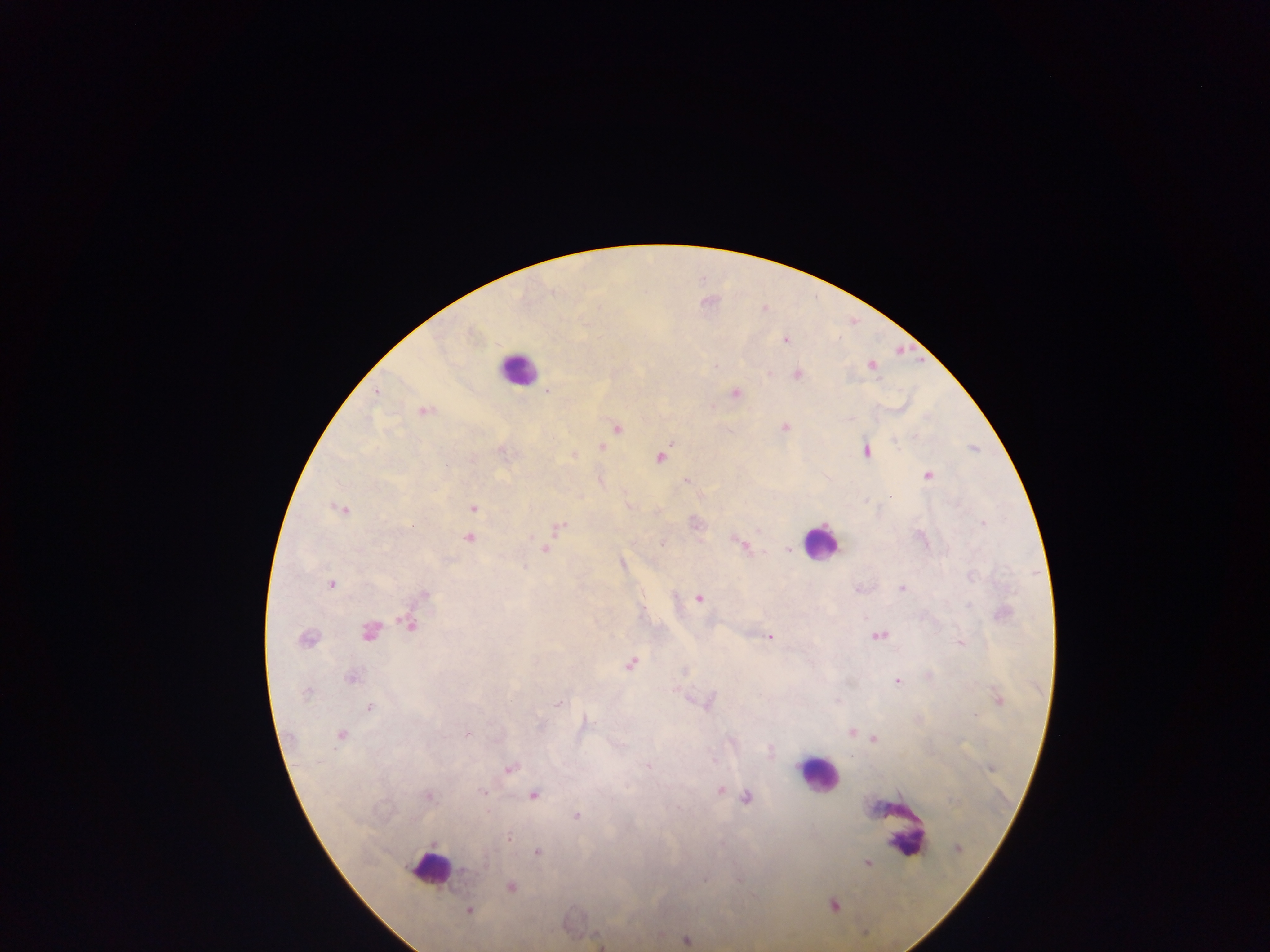
Approximate centers as [x, y] in pixels. Malaria parasite locations: [764, 309], [785, 340], [716, 365], [871, 365], [798, 374], [377, 391], [547, 391], [735, 393], [424, 412], [784, 427], [617, 428], [602, 447], [866, 452], [574, 456], [661, 457], [928, 475], [686, 481], [473, 509], [340, 510], [982, 524], [561, 526], [759, 530], [531, 537], [469, 538], [738, 542], [662, 544], [546, 548], [788, 549], [622, 564], [331, 584], [902, 588], [424, 595], [699, 598], [410, 625], [369, 631], [879, 635], [769, 637], [306, 639], [960, 643], [631, 663], [351, 677], [897, 681], [306, 692], [999, 700], [558, 705], [369, 706], [974, 715], [851, 732], [340, 735], [466, 735], [874, 738], [648, 767], [509, 769], [720, 790], [482, 792], [535, 795], [429, 796], [746, 798], [576, 816], [509, 838], [957, 849], [538, 852], [867, 862], [465, 870], [705, 879], [511, 887], [834, 906], [469, 911], [687, 940]. Leukocyte locations: [516, 368], [820, 542], [816, 775], [900, 829], [429, 869]. One field of view. Sample from Ghana. Image is 1270×952 pixels. Thick blood film. Photographed through a microscope with a mobile-phone camera.